Describe the morphology of the red blood cells.
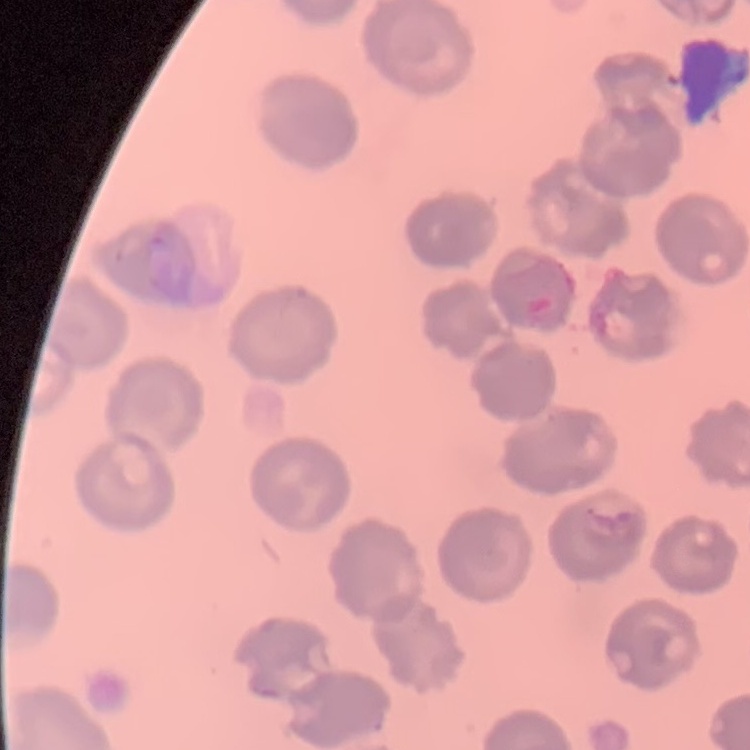

No rouleaux formation.

Thin blood smear. Field's or Giemsa stain. One tile cut from a larger photomicrograph.